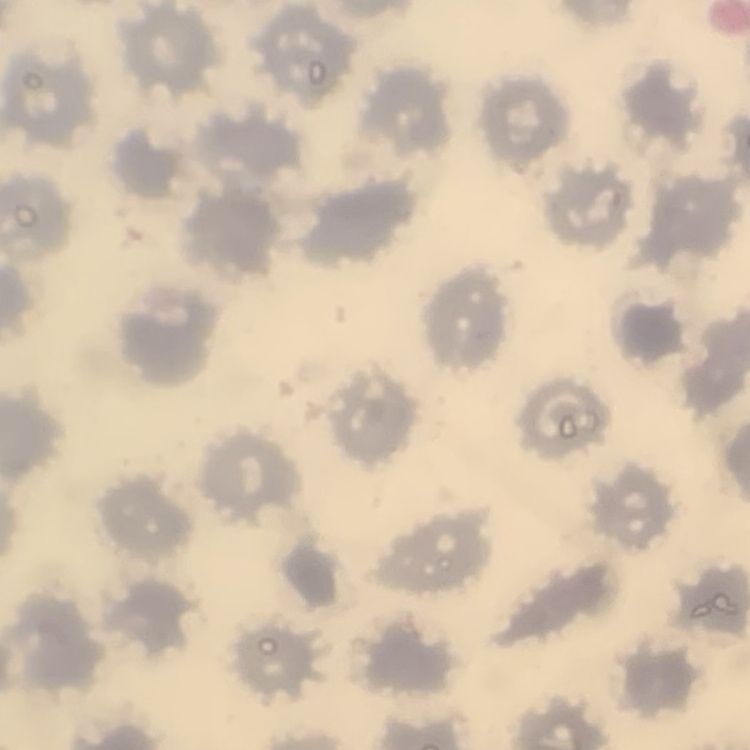

The erythrocytes exhibit no rouleaux formation. Thin blood smear. Field's or Giemsa stain. One tile cut from a larger photomicrograph.